State the blood parasite species.
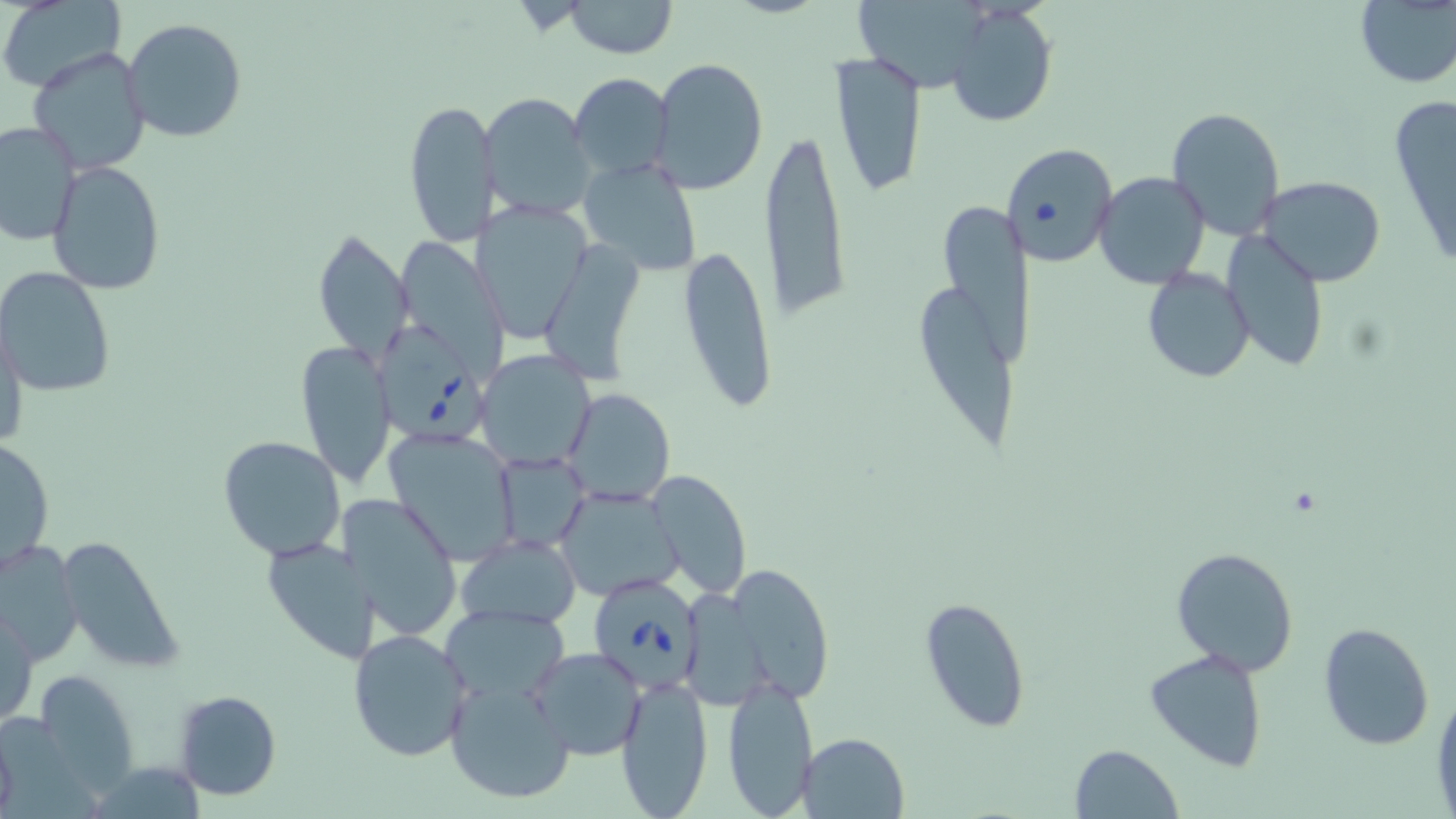

Babesia divergens.

Approximate bounding boxes as (x1, y1, x2, y2) in pixels. Babesia divergens-infected red blood cell locations: (375, 324, 489, 445), (591, 577, 704, 689). Uninfected red blood cell locations: (0, 0, 127, 93), (851, 0, 995, 95), (565, 1, 677, 58), (1353, 2, 1456, 87), (947, 5, 1058, 126), (122, 17, 248, 144), (27, 45, 152, 175), (831, 54, 928, 199), (648, 58, 770, 196), (569, 73, 674, 185), (481, 92, 596, 222), (1389, 93, 1456, 272), (402, 96, 497, 249), (1165, 105, 1286, 241), (0, 122, 80, 247), (759, 124, 853, 328), (1001, 142, 1117, 267), (578, 156, 703, 276), (46, 161, 165, 297), (1094, 171, 1211, 291), (1260, 176, 1388, 286), (935, 200, 1039, 367), (480, 201, 593, 345), (312, 229, 414, 366), (1222, 232, 1329, 373), (678, 243, 779, 413), (544, 245, 646, 381), (1, 266, 114, 397), (1141, 267, 1255, 384), (922, 288, 1018, 446), (1, 322, 26, 455), (295, 341, 395, 486), (475, 349, 597, 471), (563, 389, 677, 507), (384, 427, 522, 563), (218, 435, 347, 560), (1, 436, 54, 572), (493, 452, 590, 553), (648, 468, 752, 597), (557, 485, 684, 602), (346, 491, 461, 639), (457, 534, 582, 630), (55, 536, 184, 673), (260, 536, 375, 664), (0, 542, 81, 666), (1170, 547, 1300, 677), (718, 566, 835, 704), (918, 596, 1031, 733), (1, 600, 39, 729), (441, 605, 568, 704), (1317, 623, 1435, 750), (350, 628, 471, 762), (528, 646, 647, 760), (1143, 648, 1268, 772), (29, 669, 141, 795), (615, 675, 714, 818), (721, 676, 819, 818), (444, 678, 575, 804), (1432, 685, 1456, 817), (172, 688, 283, 802), (0, 720, 18, 818), (799, 731, 908, 817), (1068, 743, 1184, 819), (95, 768, 199, 819). Image is 1456×819 pixels. One field of a larger specimen. Captured at 1000x magnification. Light microscopy. May-Grünwald-Giemsa-stained preparation. Thin blood film.